Assess the morphology of the erythrocytes.
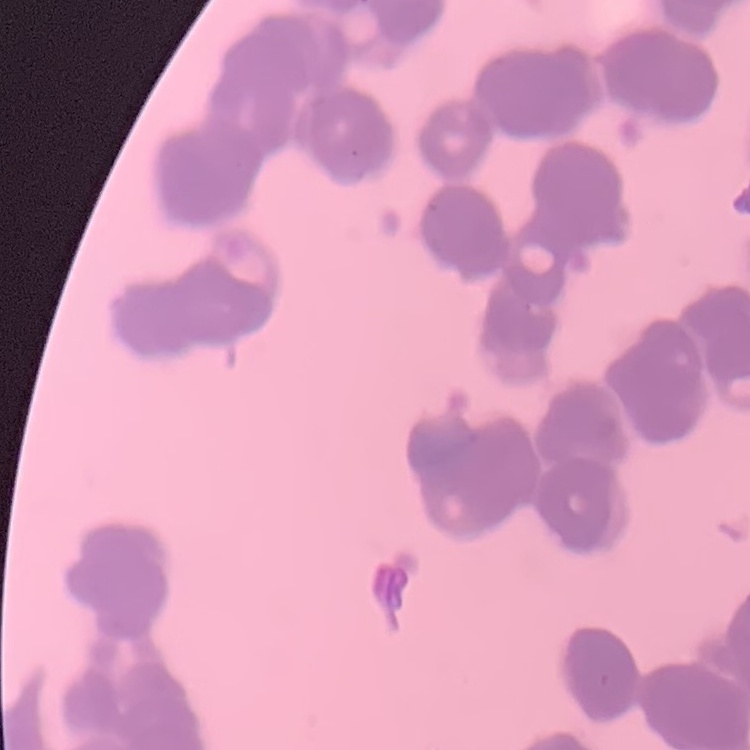
They show rouleaux formation.

preparation: thin peripheral smear
image_type: one tile cut from a larger photomicrograph
stain: Field's or Giemsa